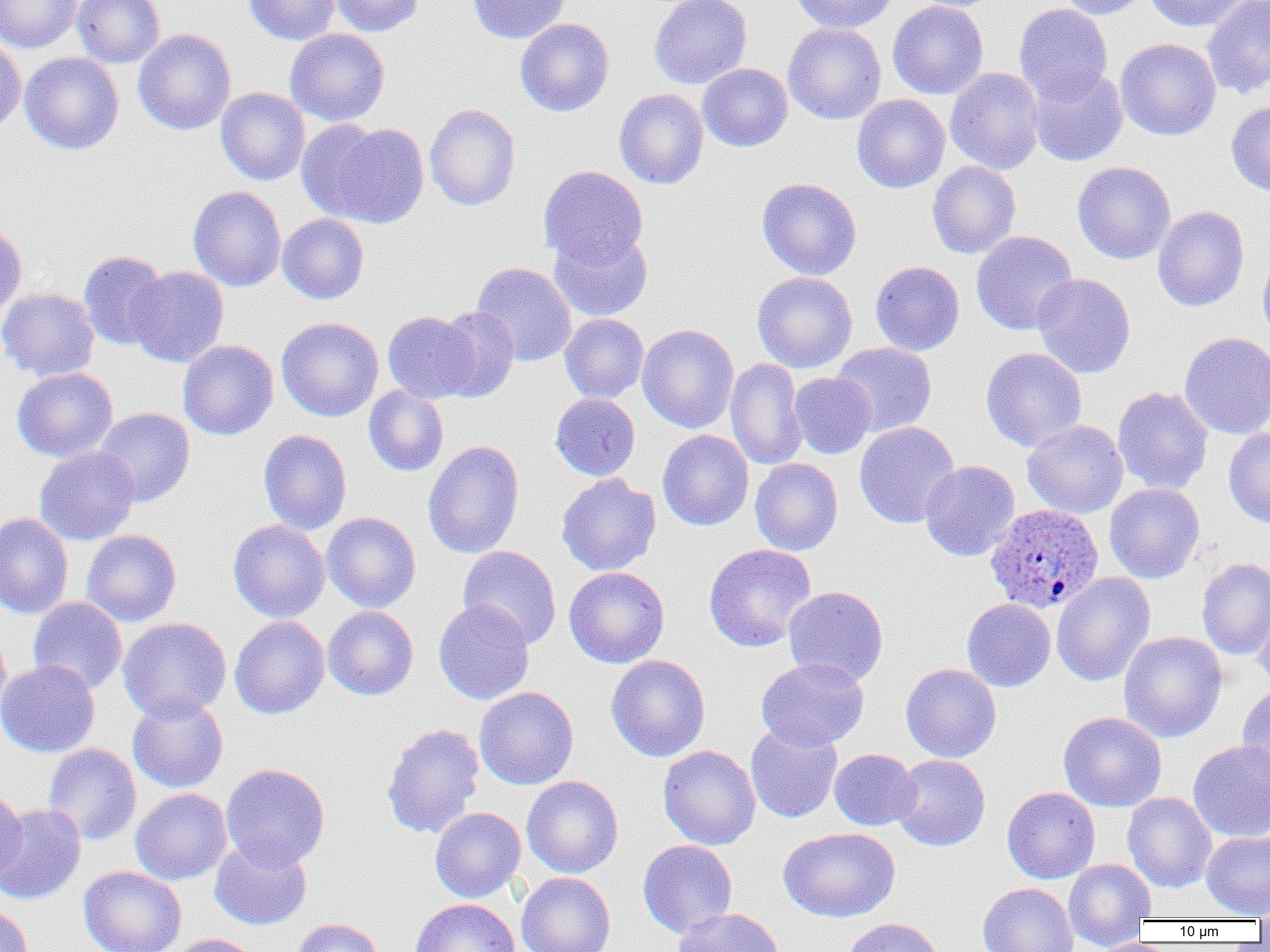 Approximate bounding boxes as [x1, y1, x2, y2] in pixels. Plasmodium ovale-infected red blood cell locations: [984, 503, 1104, 613]. Uninfected red blood cell locations: [0, 0, 82, 53], [72, 0, 165, 68], [243, 0, 341, 45], [328, 0, 425, 37], [468, 0, 572, 44], [649, 0, 752, 90], [789, 0, 898, 34], [907, 0, 1009, 12], [1056, 0, 1153, 20], [1143, 0, 1255, 32], [1202, 0, 1270, 98], [887, 1, 989, 100], [1013, 3, 1113, 103], [514, 18, 615, 117], [783, 22, 886, 124], [284, 28, 390, 127], [133, 29, 236, 135], [0, 38, 26, 133], [1115, 38, 1221, 141], [20, 52, 124, 155], [697, 63, 793, 152], [1027, 66, 1128, 166], [945, 67, 1045, 175], [216, 87, 310, 185], [614, 88, 709, 189], [852, 94, 950, 193], [1226, 100, 1270, 198], [424, 103, 521, 211], [295, 118, 388, 222], [324, 122, 430, 229], [926, 161, 1021, 259], [1072, 161, 1176, 264], [538, 165, 648, 268], [756, 177, 862, 280], [187, 186, 286, 291], [1152, 205, 1249, 312], [277, 213, 369, 304], [0, 222, 28, 320], [548, 229, 653, 322], [971, 231, 1078, 335], [1257, 249, 1270, 347], [78, 250, 171, 350], [869, 261, 965, 356], [471, 262, 577, 366], [127, 266, 229, 368], [751, 271, 858, 373], [1032, 273, 1136, 379], [0, 287, 100, 382], [433, 307, 519, 402], [382, 311, 480, 403], [559, 313, 649, 404], [276, 317, 384, 422], [637, 324, 739, 433], [1179, 331, 1270, 440], [178, 340, 279, 440], [830, 342, 937, 437], [980, 347, 1087, 452], [725, 358, 807, 471], [12, 367, 118, 463], [789, 372, 876, 459], [364, 386, 449, 477], [1112, 386, 1214, 495], [549, 393, 640, 481], [93, 407, 195, 506], [1022, 419, 1129, 519], [854, 421, 960, 528], [1223, 426, 1270, 528], [258, 429, 352, 536], [657, 429, 754, 531], [422, 440, 525, 559], [34, 446, 140, 545], [750, 458, 843, 555], [919, 460, 1020, 561], [556, 473, 661, 576], [1104, 483, 1205, 583], [322, 511, 421, 613], [0, 512, 74, 620], [227, 519, 330, 623], [81, 529, 182, 626], [703, 543, 816, 652], [458, 546, 561, 649], [1196, 558, 1270, 661], [564, 567, 670, 668], [1051, 572, 1155, 687], [783, 585, 889, 686], [27, 596, 128, 695], [1252, 597, 1270, 690], [962, 598, 1056, 692], [433, 599, 535, 705], [322, 606, 419, 700], [229, 615, 330, 719], [117, 617, 232, 722], [0, 627, 11, 722], [1119, 631, 1227, 743], [606, 654, 710, 762], [756, 657, 869, 751], [0, 659, 100, 758], [900, 663, 1001, 762], [1237, 683, 1270, 784], [474, 686, 579, 790], [127, 694, 229, 793], [1058, 711, 1166, 812], [381, 722, 485, 839], [745, 724, 843, 823], [1188, 739, 1270, 842], [42, 743, 142, 846], [658, 745, 761, 850], [828, 748, 920, 830], [890, 754, 991, 851], [221, 763, 331, 869], [522, 775, 624, 878], [1002, 786, 1100, 883], [0, 787, 27, 882], [130, 788, 232, 885], [1122, 792, 1217, 892], [0, 804, 87, 905], [429, 807, 526, 902], [778, 827, 901, 923], [1201, 830, 1270, 919], [209, 835, 312, 930], [637, 840, 738, 938], [1063, 859, 1156, 949], [78, 865, 187, 952], [516, 872, 616, 952], [651, 880, 768, 945], [978, 882, 1078, 952], [410, 898, 521, 952], [1254, 898, 1270, 932], [0, 903, 33, 952], [671, 907, 785, 952], [839, 917, 947, 952], [290, 918, 384, 952], [166, 934, 262, 952], [1090, 937, 1172, 952]. Slide-level diagnosis: Plasmodium ovale. Single field of view. Image is 1270×952 pixels. Light microscopy. 1000x magnification. Thin blood film.